Locate and identify every blood parasite.
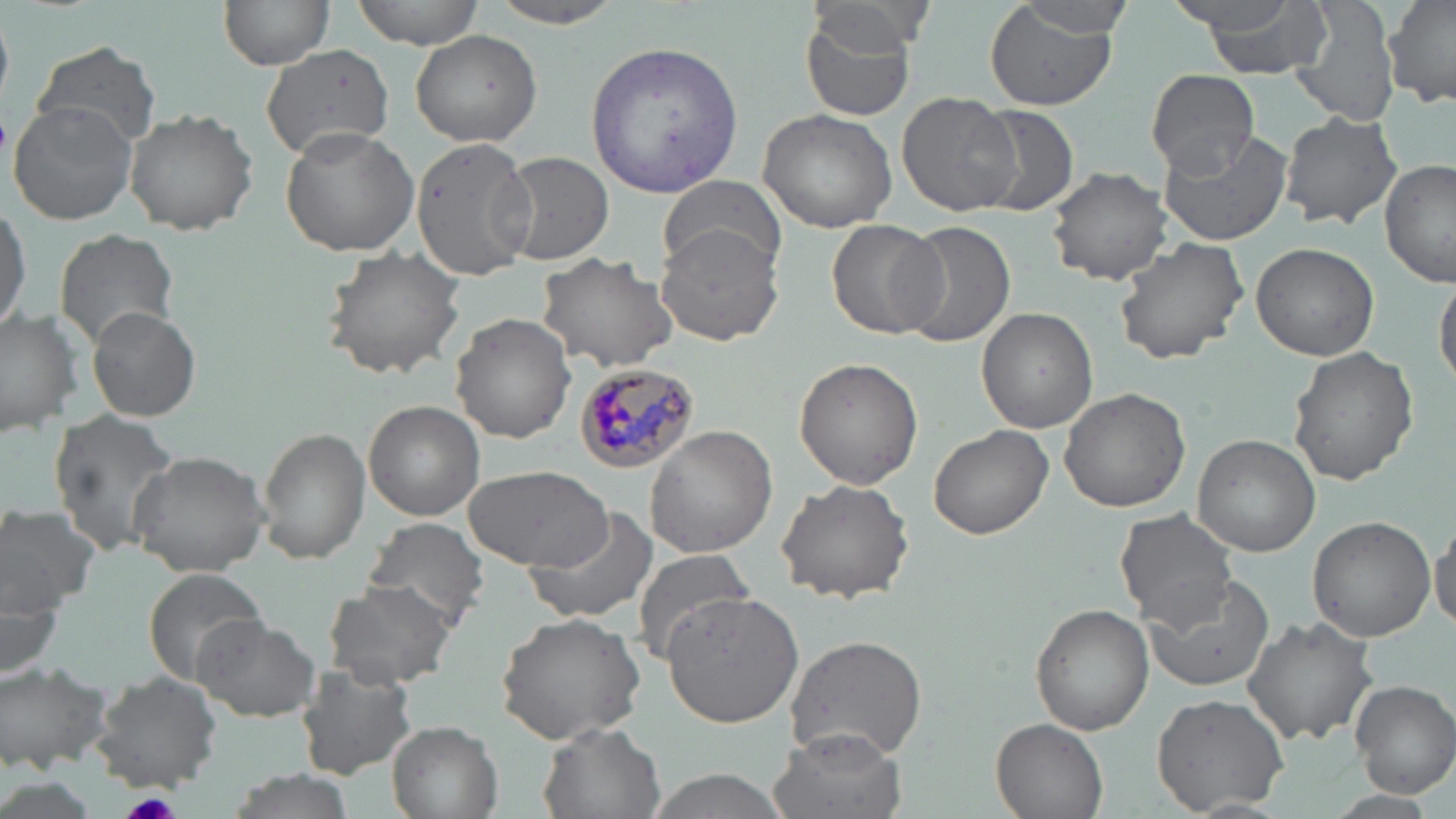
Approximate bounding boxes as (x1,y1)-(x2,y2) corner pairs in pixels.
Plasmodium malariae-infected red blood cells: (577,364)-(701,470).
No Plasmodium falciparum, Plasmodium ovale, Plasmodium vivax, Babesia divergens, or Trypanosoma brucei observed.

Uninfected red blood cell locations: (219,0)-(334,70), (351,0)-(484,47), (486,0)-(632,27), (1191,0)-(1330,77), (1290,0)-(1402,129), (1381,0)-(1456,110), (981,3)-(1120,111), (1001,4)-(1138,39), (797,6)-(919,122), (410,30)-(542,149), (586,39)-(744,197), (32,40)-(161,148), (262,44)-(394,159), (1145,69)-(1258,177), (897,93)-(1021,218), (9,102)-(136,225), (975,104)-(1081,218), (758,105)-(901,232), (124,107)-(258,236), (1278,111)-(1401,230), (1155,123)-(1296,247), (279,126)-(418,258), (411,136)-(536,281), (495,150)-(614,265), (1380,159)-(1455,287), (1046,167)-(1172,285), (657,173)-(788,277), (0,197)-(30,339), (826,217)-(949,340), (898,219)-(1016,348), (655,221)-(791,347), (54,228)-(178,349), (1113,237)-(1249,364), (1250,242)-(1380,360), (319,246)-(466,378), (537,251)-(680,371), (1435,268)-(1456,394), (0,307)-(83,436), (87,307)-(201,421), (976,307)-(1098,432), (451,313)-(577,442), (1287,347)-(1419,486), (794,357)-(923,490), (1058,387)-(1191,513), (364,400)-(484,520), (50,411)-(182,554), (927,424)-(1055,541), (257,425)-(371,565), (646,426)-(778,558), (1192,433)-(1321,555), (127,451)-(271,576), (460,465)-(612,569), (777,480)-(916,604), (0,504)-(100,618), (524,507)-(660,624), (1115,508)-(1240,631), (361,516)-(489,632), (1307,516)-(1436,642), (1430,523)-(1456,632), (629,546)-(757,666), (144,569)-(271,682), (1141,573)-(1276,696), (323,581)-(457,691), (2,587)-(65,684), (661,590)-(804,729), (1030,602)-(1156,735), (494,611)-(647,744), (1241,615)-(1379,746), (192,617)-(320,723), (784,634)-(928,762), (0,662)-(112,773), (296,663)-(416,778), (89,670)-(223,791), (1350,680)-(1456,795), (1153,692)-(1290,814), (992,717)-(1108,819), (386,721)-(503,819), (538,722)-(666,819), (768,728)-(903,819), (633,769)-(799,819). Platelet locations: (122,792)-(184,819). Slide-level diagnosis: Plasmodium malariae. One field of a larger specimen. Captured at 1000x magnification. Image is 1456×819 pixels. Thin blood film. May-Grünwald-Giemsa stain. Optical microscopy.